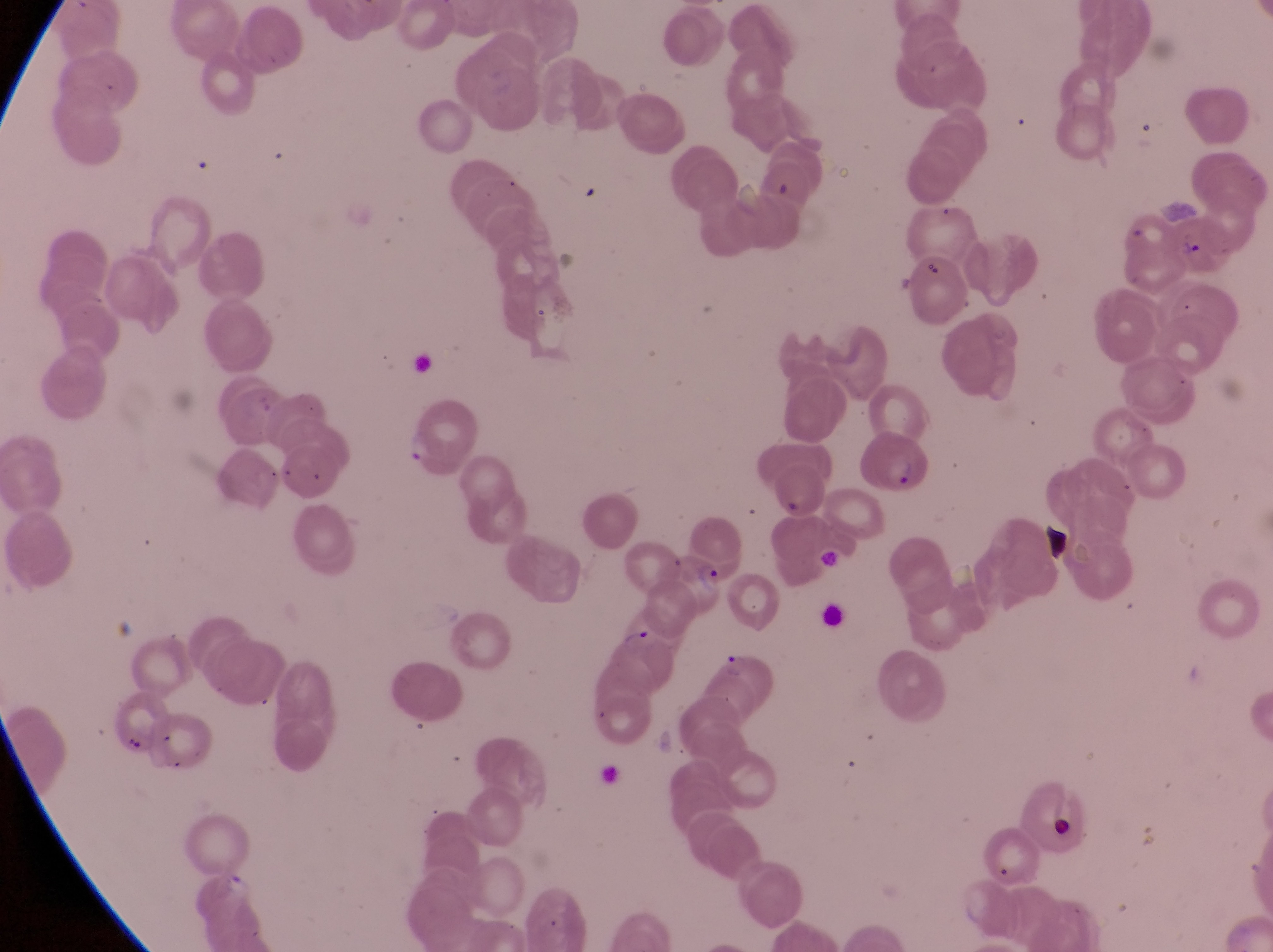
Approximate bounding boxes as left top right bottom in pixels.
Summary:
  - Parasitised red blood cell locations: 1166 213 1240 283; 858 430 928 495; 664 550 727 615
  - Trophozoite locations: 391 425 438 470; 618 622 656 658; 721 648 754 684
  - Artifact (platelet-like body, stain precipitate, or debris) locations: 898 255 943 288; 1049 817 1076 844
  - Preparation: thin blood film
  - Image size: 1273×952 pixels
  - Magnification: 1000x
  - Country: Uganda
  - Field of view: single
  - Capture: smartphone photograph through the eyepiece of an Olympus CX-23 microscope